Give the location of every parasitized red blood cell.
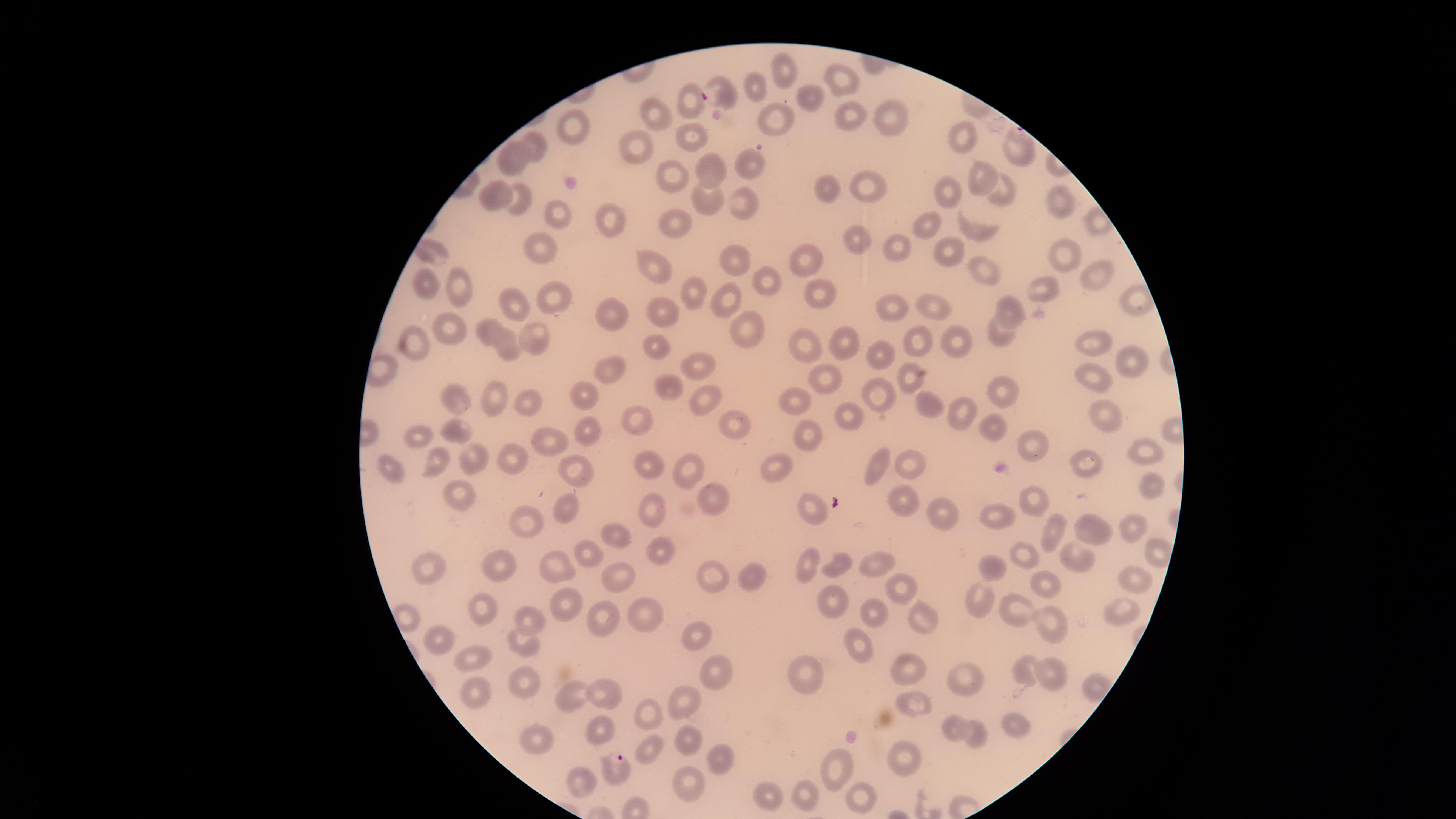
Approximate marker points, in pixels from the top-left corner.
Parasitized red blood cells: (x=717, y=93), (x=1017, y=139), (x=619, y=764).

Approximate marker points, in pixels from the top-left corner. Uninfected red blood cells: (x=787, y=67), (x=837, y=74), (x=758, y=86), (x=810, y=99), (x=690, y=103), (x=659, y=113), (x=848, y=113), (x=894, y=114), (x=775, y=120), (x=571, y=128), (x=960, y=133), (x=688, y=134), (x=632, y=146), (x=538, y=147), (x=513, y=157), (x=747, y=159), (x=704, y=167), (x=668, y=171), (x=977, y=174), (x=867, y=187), (x=1000, y=188), (x=830, y=190), (x=950, y=194), (x=494, y=195), (x=707, y=198), (x=516, y=200), (x=744, y=202), (x=1060, y=204), (x=562, y=216), (x=675, y=220), (x=926, y=220), (x=609, y=221), (x=977, y=229), (x=860, y=239), (x=948, y=248), (x=530, y=249), (x=897, y=249), (x=435, y=250), (x=1064, y=254), (x=730, y=256), (x=802, y=258), (x=654, y=267), (x=984, y=270), (x=1097, y=273), (x=761, y=277), (x=429, y=285), (x=460, y=286), (x=1045, y=286), (x=692, y=290), (x=815, y=290), (x=723, y=295), (x=556, y=300), (x=512, y=302), (x=1131, y=303), (x=896, y=306), (x=666, y=307), (x=934, y=307), (x=1013, y=307), (x=616, y=315), (x=453, y=325), (x=489, y=329), (x=744, y=329), (x=997, y=334), (x=953, y=338), (x=537, y=339), (x=847, y=341), (x=915, y=341), (x=1090, y=342), (x=801, y=343), (x=420, y=344), (x=654, y=346), (x=505, y=348), (x=880, y=358), (x=1131, y=362), (x=697, y=364), (x=611, y=366), (x=1094, y=376), (x=906, y=378), (x=822, y=380), (x=662, y=383), (x=876, y=386), (x=1004, y=390), (x=497, y=393), (x=585, y=394), (x=695, y=394), (x=526, y=398), (x=796, y=401), (x=457, y=402), (x=926, y=403), (x=965, y=409), (x=849, y=414), (x=1103, y=414), (x=638, y=421), (x=989, y=423), (x=741, y=425), (x=589, y=429), (x=457, y=430), (x=803, y=431), (x=420, y=433), (x=555, y=438), (x=1033, y=443), (x=1145, y=448), (x=512, y=454), (x=474, y=456), (x=435, y=459), (x=1090, y=460), (x=882, y=462), (x=913, y=462), (x=654, y=463), (x=779, y=466), (x=692, y=467), (x=577, y=468), (x=395, y=469), (x=1158, y=488), (x=458, y=492), (x=708, y=494), (x=899, y=494), (x=1034, y=498), (x=811, y=504), (x=566, y=506), (x=656, y=509), (x=939, y=512), (x=1003, y=515), (x=527, y=522), (x=1053, y=522), (x=1088, y=525), (x=1130, y=527), (x=613, y=535), (x=656, y=545), (x=1156, y=550), (x=590, y=551), (x=1029, y=557), (x=1078, y=557), (x=501, y=560), (x=807, y=561), (x=880, y=561), (x=840, y=562), (x=423, y=565), (x=992, y=567), (x=561, y=568), (x=708, y=569), (x=615, y=571), (x=749, y=576), (x=1049, y=577), (x=1136, y=579), (x=903, y=592), (x=565, y=596), (x=976, y=598), (x=833, y=599), (x=1018, y=604), (x=479, y=608), (x=638, y=611), (x=878, y=612), (x=1123, y=613), (x=1046, y=615), (x=532, y=616), (x=921, y=616), (x=598, y=621), (x=695, y=631), (x=442, y=638), (x=519, y=644), (x=857, y=644), (x=472, y=656), (x=912, y=668), (x=714, y=669), (x=1049, y=669), (x=1029, y=671), (x=799, y=676), (x=517, y=679), (x=966, y=679), (x=1090, y=685), (x=478, y=691), (x=566, y=693), (x=603, y=695), (x=688, y=700), (x=915, y=701), (x=651, y=714), (x=1015, y=723), (x=954, y=727), (x=602, y=730), (x=976, y=733), (x=545, y=740), (x=688, y=740), (x=651, y=746), (x=906, y=756), (x=717, y=759), (x=835, y=765), (x=580, y=776), (x=689, y=784), (x=768, y=791), (x=855, y=792), (x=806, y=794). Circular visible region. Single field of view. Image is 1456×819 pixels. Photographed with a smartphone camera through the microscope eyepiece. Giemsa stain. Species: Plasmodium falciparum. Thin blood film.